Locate every Plasmodium parasite.
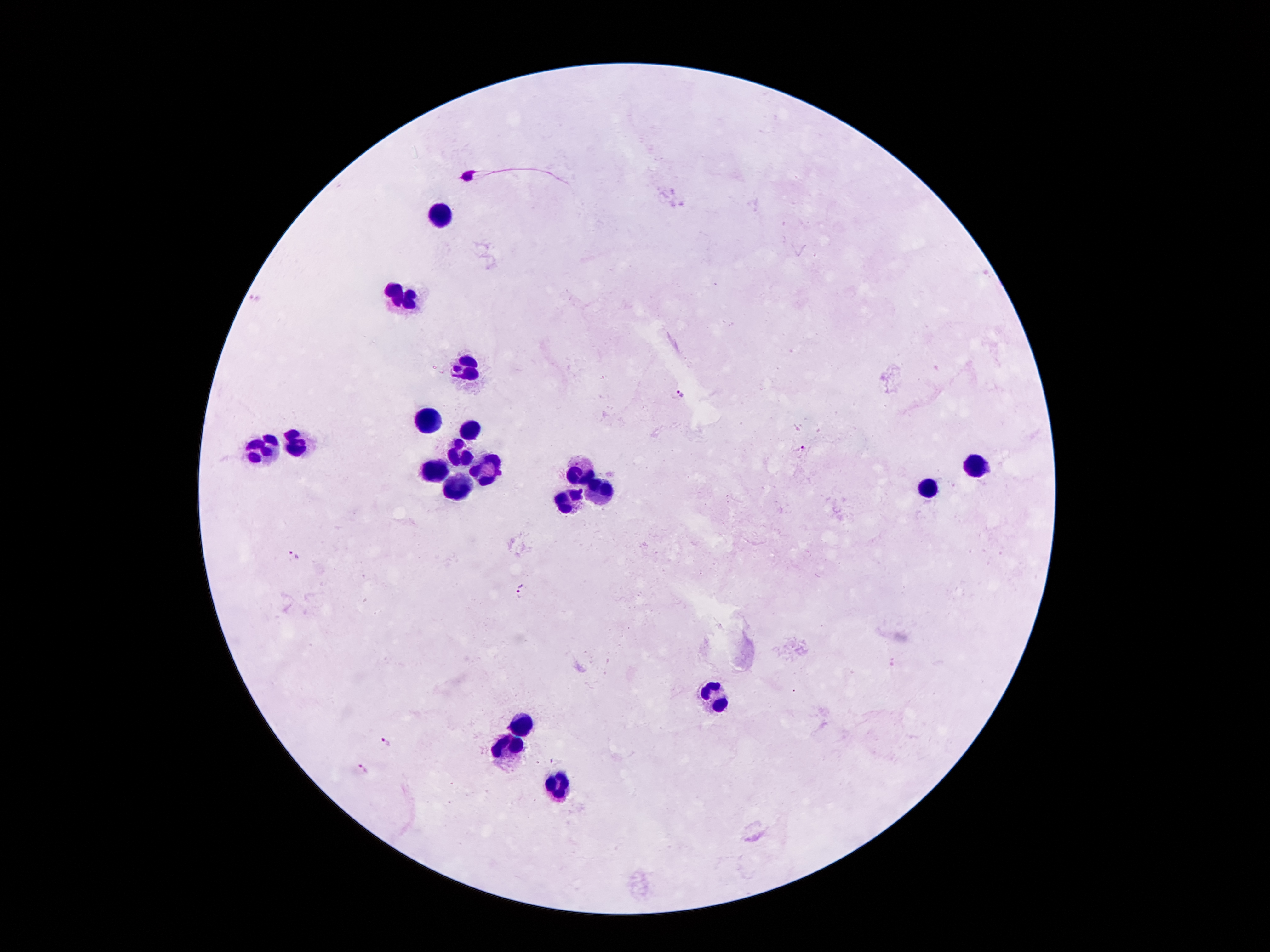
Approximate object centers, in pixels from the top-left corner.
Plasmodium parasites: (x=682, y=394), (x=803, y=448), (x=294, y=555), (x=519, y=589), (x=387, y=742), (x=558, y=759), (x=361, y=769).

Summary:
  - Leukocyte locations: (x=440, y=214), (x=398, y=300), (x=471, y=371), (x=424, y=423), (x=469, y=431), (x=297, y=442), (x=265, y=446), (x=465, y=454), (x=974, y=466), (x=489, y=468), (x=431, y=469), (x=582, y=472), (x=463, y=488), (x=928, y=488), (x=602, y=494), (x=566, y=500), (x=712, y=698), (x=518, y=727), (x=505, y=750), (x=557, y=785)
  - Preparation: thick peripheral-blood smear
  - Field of view: single
  - Patient malaria status: infected with Plasmodium falciparum
  - Image size: 1270×952 pixels
  - Stain: Giemsa
  - Magnification: 100x
  - Capture: smartphone through the microscope eyepiece